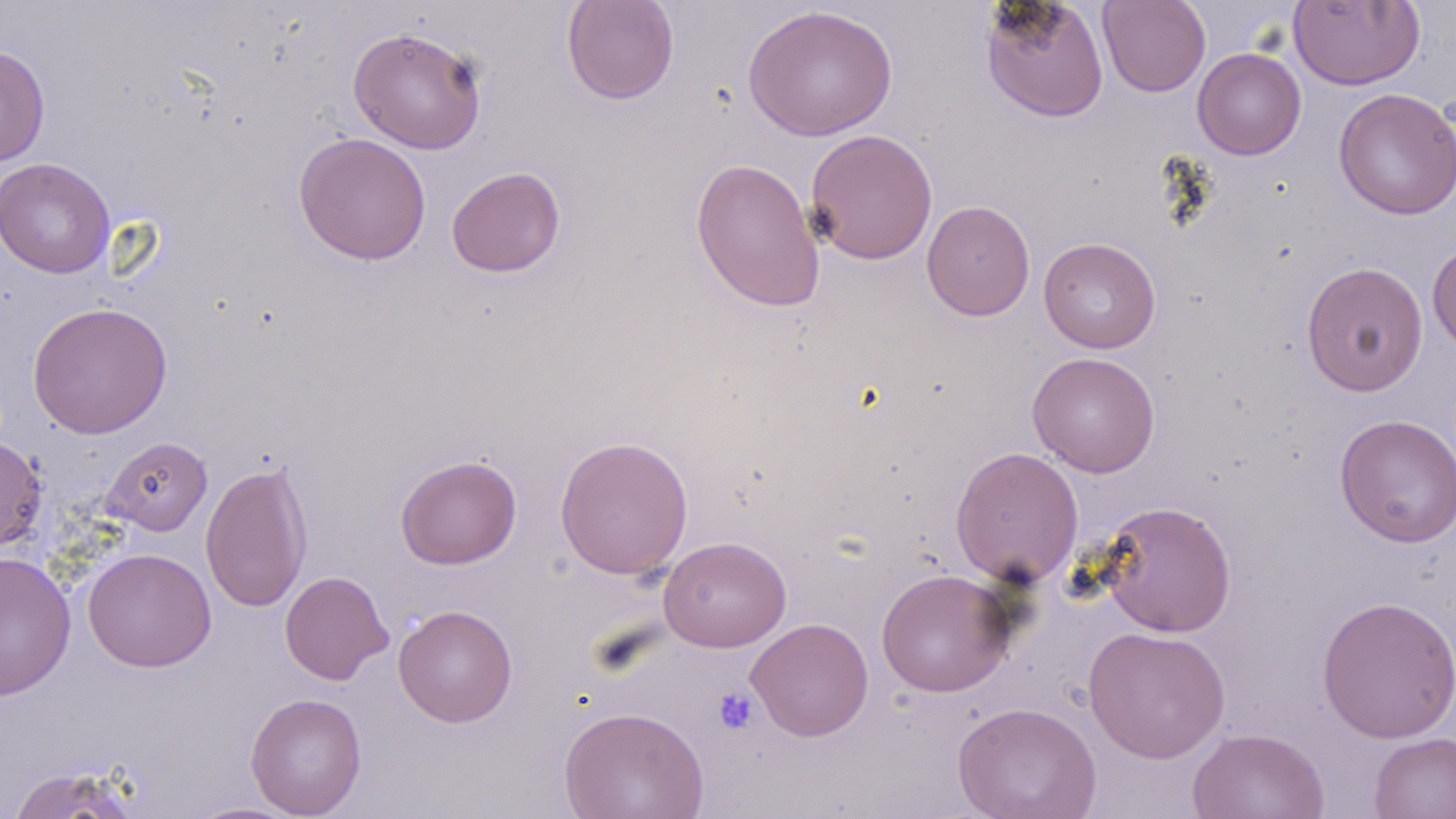
slide-level diagnosis = negative for blood parasites
modality = light microscopy
preparation = thin blood film
stain = May-Grünwald-Giemsa
platelet locations = approximate bounding boxes as named x1/y1/x2/y2 corners in pixels: (x1=713, y1=688, x2=759, y2=734)
magnification = 1000x
image size = 1456×819 pixels
uninfected red blood cell locations = approximate bounding boxes as named x1/y1/x2/y2 corners in pixels: (x1=562, y1=0, x2=679, y2=104), (x1=979, y1=0, x2=1110, y2=123), (x1=1098, y1=0, x2=1211, y2=97), (x1=1288, y1=1, x2=1425, y2=90), (x1=743, y1=4, x2=898, y2=141), (x1=347, y1=26, x2=488, y2=154), (x1=0, y1=44, x2=50, y2=167), (x1=1192, y1=47, x2=1306, y2=160), (x1=1333, y1=87, x2=1456, y2=220), (x1=804, y1=128, x2=938, y2=265), (x1=293, y1=132, x2=431, y2=265), (x1=690, y1=156, x2=826, y2=313), (x1=0, y1=157, x2=115, y2=279), (x1=446, y1=166, x2=565, y2=277), (x1=922, y1=200, x2=1035, y2=321), (x1=1039, y1=236, x2=1161, y2=353), (x1=1427, y1=240, x2=1456, y2=357), (x1=1301, y1=261, x2=1428, y2=396), (x1=27, y1=301, x2=173, y2=438), (x1=1027, y1=351, x2=1160, y2=477), (x1=1335, y1=413, x2=1456, y2=547), (x1=554, y1=435, x2=694, y2=579), (x1=0, y1=436, x2=46, y2=551), (x1=102, y1=436, x2=212, y2=536), (x1=950, y1=446, x2=1084, y2=587), (x1=395, y1=454, x2=522, y2=570), (x1=200, y1=458, x2=313, y2=613), (x1=1097, y1=500, x2=1237, y2=637), (x1=658, y1=535, x2=792, y2=652), (x1=83, y1=548, x2=216, y2=672), (x1=1, y1=551, x2=76, y2=700), (x1=875, y1=569, x2=1015, y2=697), (x1=279, y1=570, x2=394, y2=685), (x1=1316, y1=594, x2=1456, y2=743), (x1=393, y1=604, x2=518, y2=727), (x1=745, y1=617, x2=874, y2=741), (x1=1083, y1=625, x2=1230, y2=763), (x1=245, y1=692, x2=367, y2=818), (x1=952, y1=701, x2=1102, y2=819), (x1=558, y1=705, x2=709, y2=819), (x1=1187, y1=727, x2=1330, y2=819), (x1=1368, y1=731, x2=1456, y2=819), (x1=4, y1=765, x2=148, y2=818), (x1=181, y1=801, x2=307, y2=818)
field of view = single